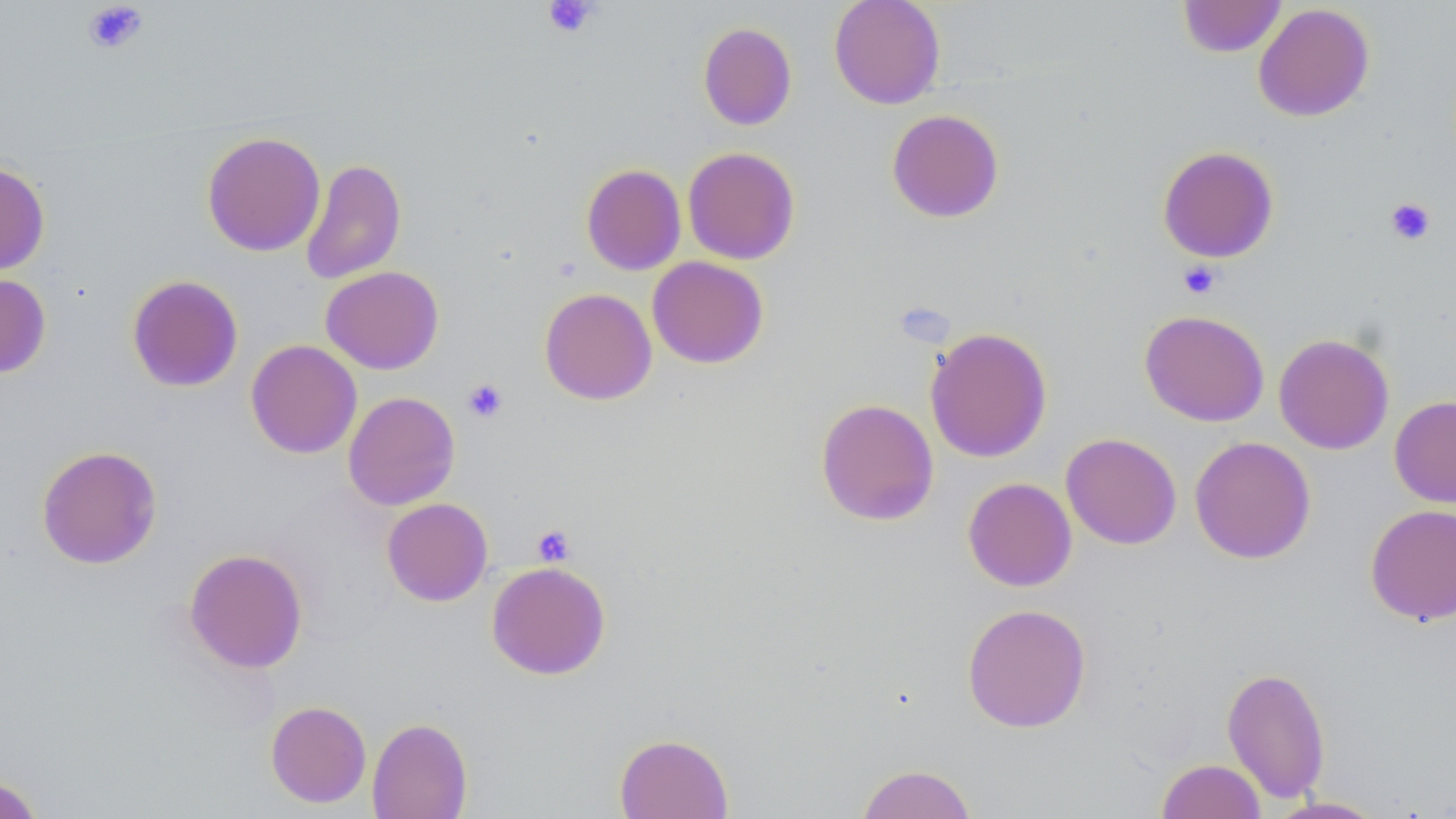
slide-level diagnosis = negative for blood parasites
stain = May-Grünwald-Giemsa
platelet locations = approximate bounding boxes as (x1,y1)-(x2,y2) corner pairs in pixels: (542,0)-(600,38), (82,1)-(149,54), (1385,198)-(1436,245), (1177,261)-(1221,299), (462,379)-(508,422), (532,525)-(576,567)
uninfected red blood cell locations = approximate bounding boxes as (x1,y1)-(x2,y2) corner pairs in pixels: (829,0)-(946,109), (1178,0)-(1287,58), (1253,3)-(1375,122), (698,22)-(797,130), (886,109)-(1004,223), (202,131)-(325,256), (1157,146)-(1279,263), (683,147)-(800,264), (299,158)-(406,284), (0,160)-(50,275), (581,164)-(686,275), (647,256)-(768,368), (320,266)-(444,374), (0,273)-(51,378), (126,274)-(243,392), (539,287)-(657,405), (1139,309)-(1269,427), (924,327)-(1052,463), (1273,333)-(1395,454), (246,340)-(362,459), (343,391)-(460,510), (1389,395)-(1456,508), (815,398)-(939,526), (1061,432)-(1182,550), (1189,436)-(1316,564), (36,445)-(162,569), (962,477)-(1077,591), (382,498)-(493,605), (1365,504)-(1456,626), (184,548)-(308,673), (486,561)-(611,680), (962,603)-(1091,732), (1222,666)-(1331,802), (265,701)-(372,808), (366,717)-(473,819), (614,732)-(734,818), (1156,758)-(1267,819), (855,763)-(978,819), (0,774)-(44,819), (1265,796)-(1389,818)
preparation = thin blood film
field of view = one of a larger specimen
image size = 1456×819 pixels
magnification = 1000x
modality = optical microscopy